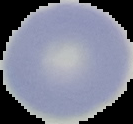

From a thin blood smear. Segmented cell region on a black background. Result: no Plasmodium parasites seen. Image is 133×124 pixels.